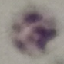

Summary:
  - Result: negative for malaria parasites
  - Preparation: thin blood film
  - Capture: smartphone camera at the microscope eyepiece
  - Image type: cell patch, automatically extracted from a larger field of view and resized to 64 × 64 pixels
  - Stain: Giemsa